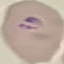
Summary:
  - Result: malaria parasites detected
  - Preparation: thin smear
  - Capture: smartphone camera at the microscope eyepiece
  - Image type: automatically extracted cell patch, resized to 64 × 64 pixels
  - Stain: Giemsa